Classify this cell by malaria status.
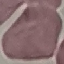

It is uninfected.

{
  "stain": "Giemsa",
  "capture": "smartphone through the microscope eyepiece",
  "preparation": "thin blood smear",
  "image_type": "cell patch, automatically extracted from a larger field of view and resized to 64 × 64 pixels"
}